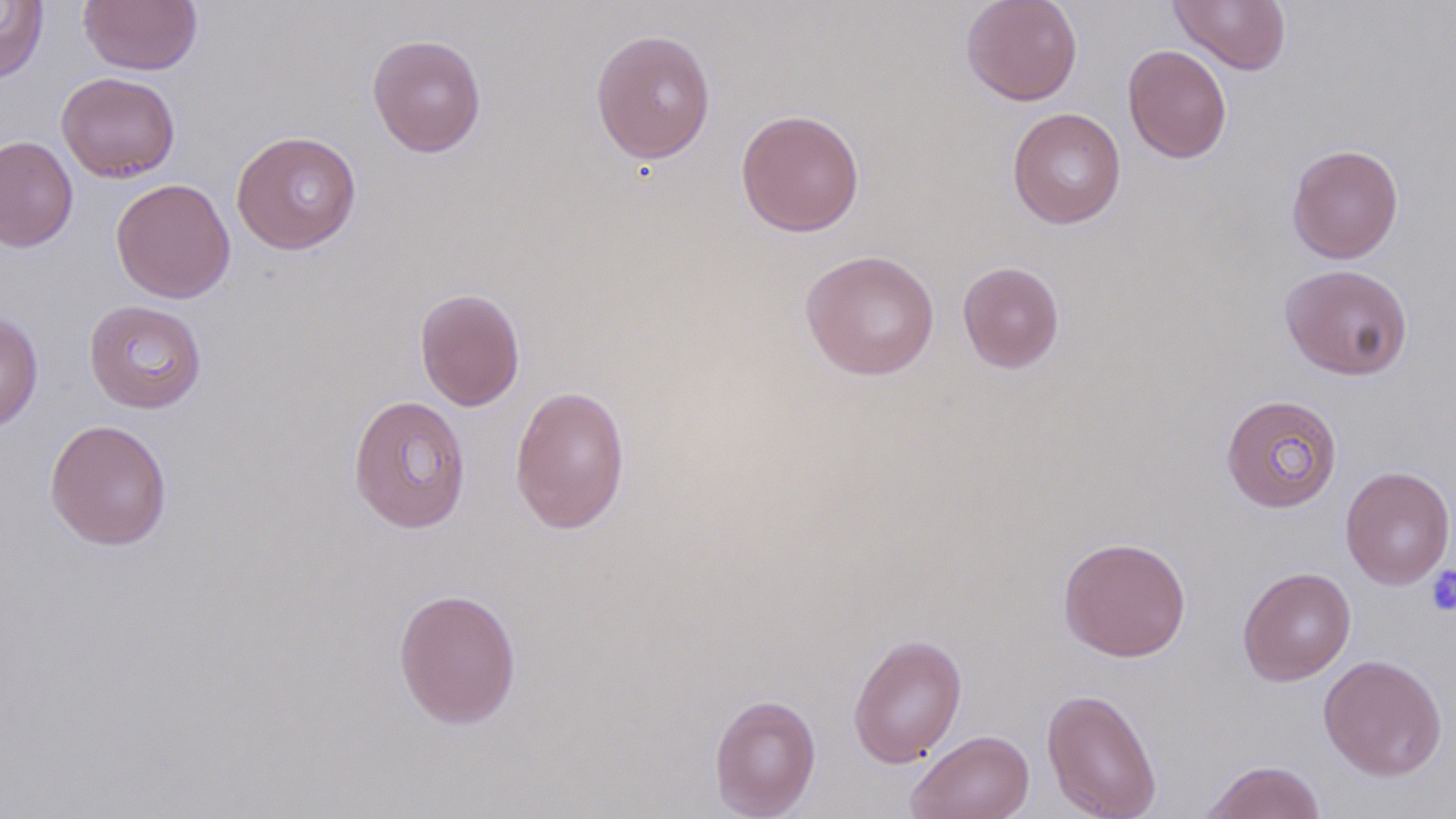
slide-level diagnosis = negative for blood parasites
preparation = thin blood smear
magnification = 1000x
field of view = single
modality = optical microscopy
image size = 1456×819 pixels
platelet locations = approximate bounding boxes as named x1/y1/x2/y2 corners in pixels: (x1=1425, y1=564, x2=1456, y2=616)
uninfected red blood cell locations = approximate bounding boxes as named x1/y1/x2/y2 corners in pixels: (x1=79, y1=0, x2=202, y2=76), (x1=961, y1=0, x2=1083, y2=106), (x1=1170, y1=0, x2=1291, y2=75), (x1=0, y1=1, x2=49, y2=85), (x1=590, y1=28, x2=716, y2=165), (x1=367, y1=33, x2=487, y2=158), (x1=1123, y1=44, x2=1231, y2=164), (x1=56, y1=71, x2=181, y2=182), (x1=1007, y1=107, x2=1126, y2=228), (x1=735, y1=108, x2=865, y2=237), (x1=231, y1=130, x2=362, y2=254), (x1=0, y1=136, x2=79, y2=252), (x1=1286, y1=143, x2=1403, y2=263), (x1=111, y1=178, x2=236, y2=304), (x1=800, y1=249, x2=940, y2=380), (x1=957, y1=261, x2=1065, y2=373), (x1=1279, y1=263, x2=1414, y2=380), (x1=414, y1=287, x2=525, y2=411), (x1=84, y1=299, x2=207, y2=413), (x1=0, y1=312, x2=43, y2=433), (x1=509, y1=385, x2=631, y2=535), (x1=348, y1=394, x2=471, y2=533), (x1=1221, y1=394, x2=1343, y2=513), (x1=44, y1=419, x2=173, y2=551), (x1=1340, y1=466, x2=1455, y2=589), (x1=1058, y1=536, x2=1192, y2=662), (x1=1237, y1=566, x2=1356, y2=686), (x1=392, y1=587, x2=523, y2=730), (x1=848, y1=633, x2=967, y2=768), (x1=1318, y1=654, x2=1448, y2=781), (x1=1041, y1=687, x2=1162, y2=819), (x1=709, y1=693, x2=821, y2=818), (x1=906, y1=729, x2=1035, y2=819), (x1=1199, y1=759, x2=1327, y2=818)
stain = May-Grünwald-Giemsa